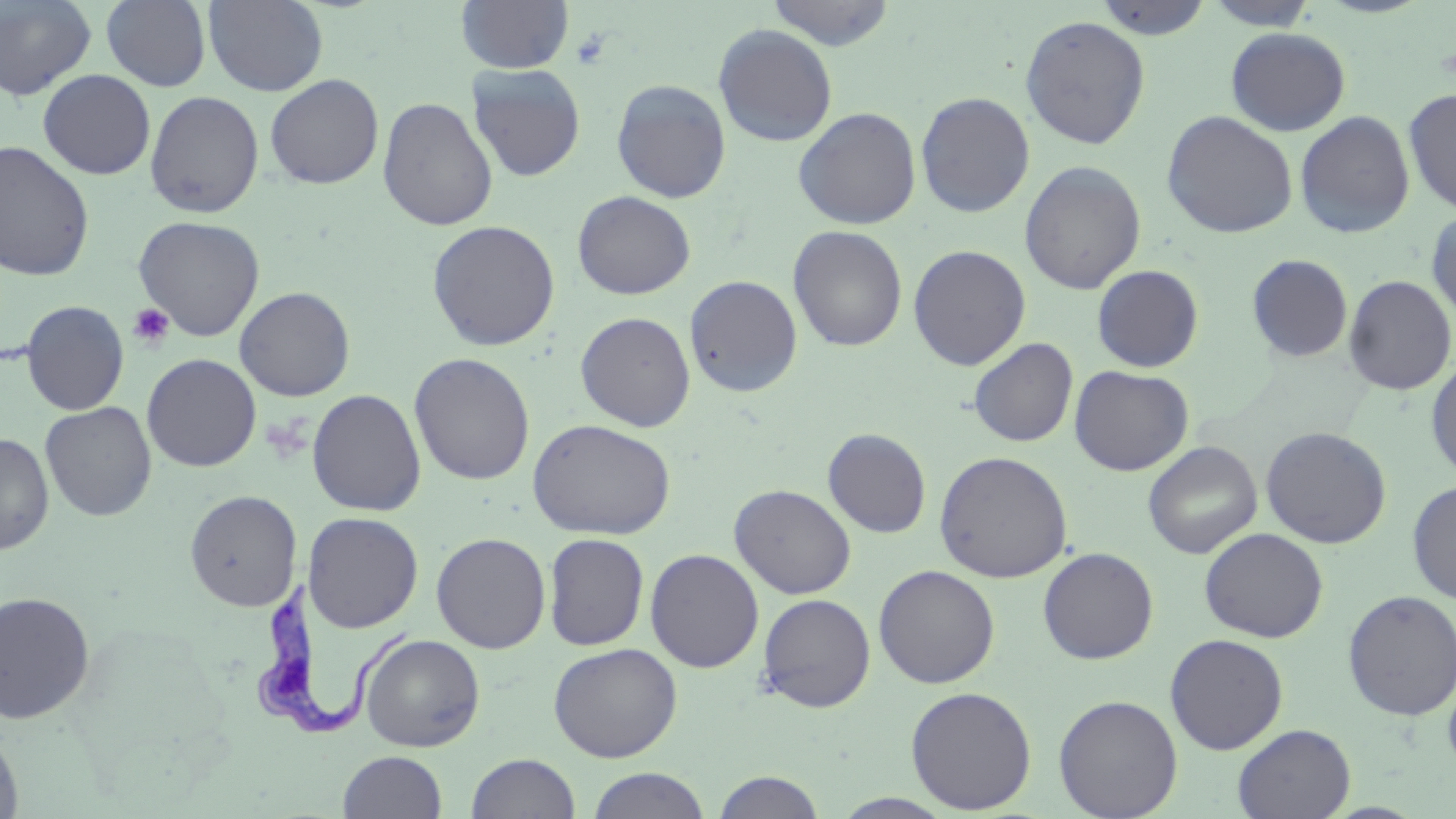
slide_level_diagnosis: Trypanosoma brucei
modality: optical microscopy
stain: May-Grünwald-Giemsa
preparation: thin blood film
uninfected_red_blood_cell_locations: 'approximate bounding boxes as named x1/y1/x2/y2 corners in pixels: (x1=0, y1=0, x2=98, y2=102), (x1=101, y1=0, x2=212, y2=91), (x1=203, y1=0, x2=329, y2=97), (x1=456, y1=0, x2=575, y2=74), (x1=765, y1=0, x2=897, y2=50), (x1=1092, y1=0, x2=1215, y2=40), (x1=1203, y1=1, x2=1319, y2=30), (x1=1019, y1=15, x2=1151, y2=150), (x1=713, y1=24, x2=838, y2=147), (x1=1226, y1=27, x2=1352, y2=136), (x1=467, y1=64, x2=586, y2=182), (x1=37, y1=69, x2=156, y2=180), (x1=265, y1=74, x2=384, y2=189), (x1=610, y1=78, x2=732, y2=202), (x1=1403, y1=87, x2=1456, y2=215), (x1=144, y1=90, x2=264, y2=218), (x1=915, y1=91, x2=1035, y2=218), (x1=377, y1=97, x2=497, y2=231), (x1=792, y1=106, x2=921, y2=229), (x1=1161, y1=110, x2=1298, y2=238), (x1=1294, y1=110, x2=1415, y2=239), (x1=0, y1=141, x2=95, y2=282), (x1=1020, y1=160, x2=1146, y2=295), (x1=572, y1=190, x2=696, y2=300), (x1=1425, y1=207, x2=1456, y2=325), (x1=132, y1=215, x2=266, y2=341), (x1=426, y1=220, x2=560, y2=351), (x1=787, y1=225, x2=908, y2=351), (x1=908, y1=244, x2=1031, y2=370), (x1=1246, y1=253, x2=1353, y2=363), (x1=1092, y1=264, x2=1204, y2=372), (x1=683, y1=275, x2=803, y2=398), (x1=1342, y1=275, x2=1455, y2=396), (x1=235, y1=286, x2=355, y2=401), (x1=21, y1=300, x2=129, y2=415), (x1=575, y1=311, x2=696, y2=431), (x1=968, y1=337, x2=1079, y2=447), (x1=142, y1=353, x2=261, y2=472), (x1=409, y1=353, x2=535, y2=485), (x1=1425, y1=354, x2=1456, y2=482), (x1=1069, y1=365, x2=1193, y2=476), (x1=307, y1=389, x2=426, y2=517), (x1=40, y1=401, x2=157, y2=522), (x1=527, y1=418, x2=676, y2=540), (x1=1260, y1=426, x2=1391, y2=548), (x1=823, y1=428, x2=931, y2=538), (x1=0, y1=432, x2=54, y2=555), (x1=1143, y1=440, x2=1262, y2=559), (x1=934, y1=450, x2=1072, y2=583), (x1=1407, y1=479, x2=1456, y2=604), (x1=729, y1=484, x2=856, y2=599), (x1=185, y1=490, x2=302, y2=611), (x1=303, y1=512, x2=423, y2=632), (x1=1199, y1=527, x2=1328, y2=643), (x1=431, y1=532, x2=551, y2=653), (x1=543, y1=533, x2=649, y2=651), (x1=1037, y1=547, x2=1159, y2=664), (x1=645, y1=548, x2=764, y2=672), (x1=873, y1=564, x2=999, y2=689), (x1=1342, y1=589, x2=1456, y2=721), (x1=0, y1=591, x2=95, y2=723), (x1=757, y1=593, x2=876, y2=712), (x1=1164, y1=633, x2=1289, y2=754), (x1=359, y1=634, x2=485, y2=752), (x1=548, y1=642, x2=683, y2=762), (x1=1442, y1=671, x2=1456, y2=780), (x1=905, y1=685, x2=1037, y2=814), (x1=1053, y1=694, x2=1183, y2=818), (x1=1232, y1=723, x2=1356, y2=819), (x1=0, y1=730, x2=23, y2=819), (x1=338, y1=750, x2=447, y2=818), (x1=467, y1=752, x2=580, y2=819), (x1=586, y1=767, x2=711, y2=819), (x1=711, y1=770, x2=826, y2=818), (x1=830, y1=793, x2=957, y2=818)'
field_of_view: single
trypanosoma_brucei_locations: 'approximate bounding boxes as named x1/y1/x2/y2 corners in pixels: (x1=243, y1=579, x2=422, y2=737)'
image_size: 1456×819 pixels
platelet_locations: 'approximate bounding boxes as named x1/y1/x2/y2 corners in pixels: (x1=570, y1=28, x2=611, y2=71), (x1=128, y1=304, x2=174, y2=350)'
magnification: 1000x